Give the position of every malaria parasite and every leukocyte.
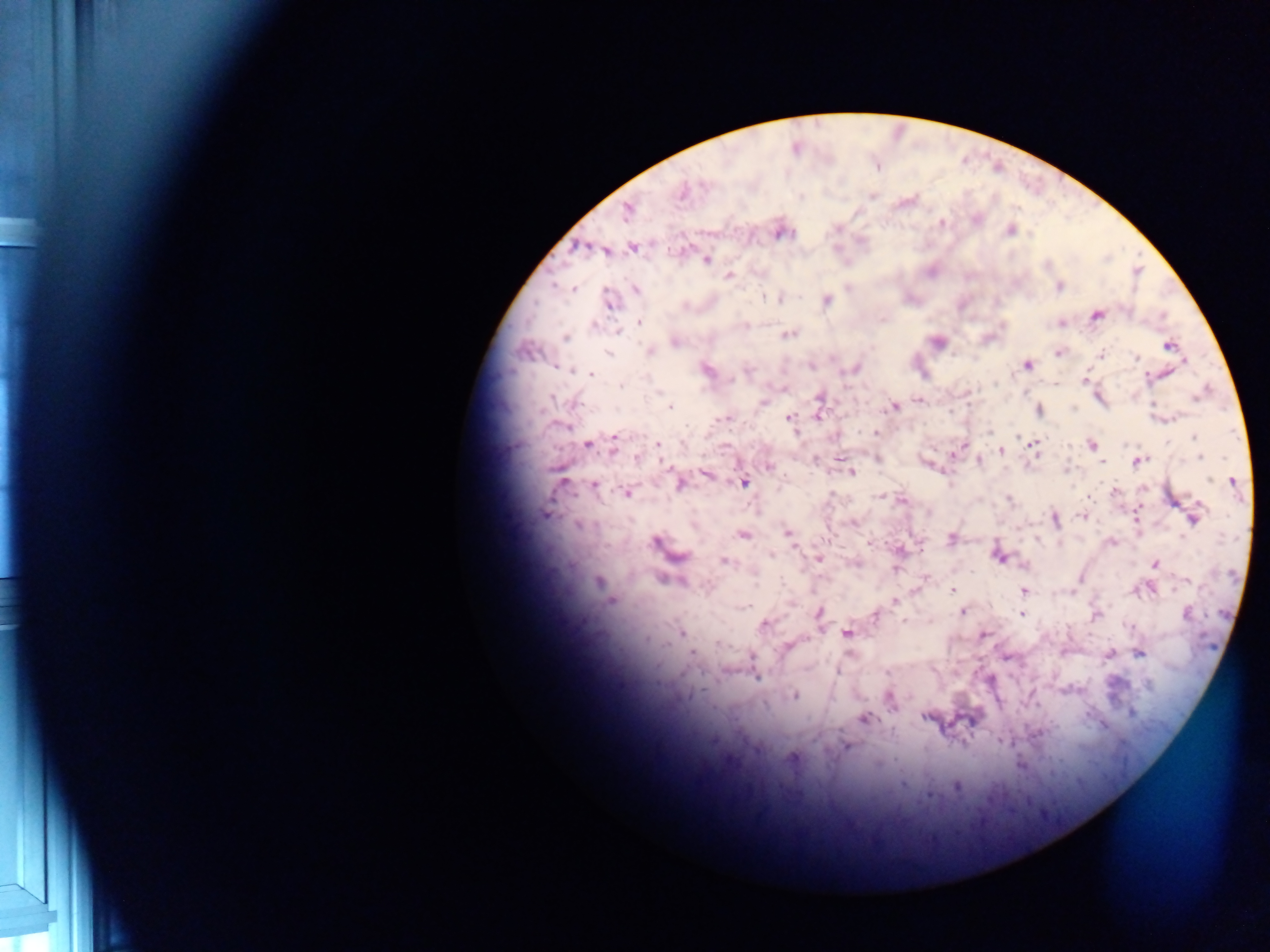

Approximate centers as {x, y} in pixels.
Malaria parasites: {681, 193}, {870, 194}, {905, 201}, {627, 210}, {975, 218}, {941, 223}, {1010, 229}, {779, 231}, {583, 247}, {604, 248}, {633, 248}, {706, 259}, {728, 275}, {1059, 286}, {635, 288}, {572, 289}, {779, 298}, {825, 300}, {608, 301}, {1096, 315}, {1060, 321}, {638, 322}, {745, 325}, {788, 334}, {566, 337}, {675, 341}, {937, 342}, {1168, 345}, {649, 351}, {1059, 351}, {607, 352}, {1101, 355}, {1135, 358}, {1027, 364}, {810, 365}, {854, 368}, {706, 369}, {590, 374}, {1084, 381}, {1054, 383}, {782, 388}, {820, 397}, {919, 400}, {763, 403}, {892, 406}, {669, 407}, {1038, 410}, {819, 414}, {726, 417}, {790, 418}, {875, 433}, {587, 444}, {656, 444}, {1091, 444}, {613, 445}, {1032, 445}, {1001, 449}, {1200, 456}, {637, 457}, {837, 457}, {876, 458}, {979, 460}, {1138, 461}, {926, 462}, {1102, 462}, {769, 466}, {851, 472}, {705, 474}, {1233, 481}, {678, 482}, {744, 482}, {593, 485}, {1114, 491}, {626, 492}, {881, 496}, {1172, 498}, {902, 500}, {544, 514}, {1136, 515}, {1083, 516}, {1194, 517}, {1055, 519}, {852, 523}, {787, 533}, {742, 534}, {951, 538}, {869, 541}, {1111, 542}, {656, 543}, {899, 550}, {999, 556}, {819, 557}, {724, 560}, {856, 563}, {1155, 564}, {896, 568}, {924, 577}, {668, 579}, {598, 582}, {952, 590}, {1023, 590}, {610, 601}, {894, 601}, {746, 605}, {963, 611}, {818, 613}, {1019, 613}, {874, 614}, {1095, 616}, {904, 621}, {763, 625}, {681, 632}, {847, 633}, {984, 634}, {787, 646}, {850, 651}, {1139, 653}, {693, 654}, {1109, 654}, {1004, 656}, {755, 676}, {794, 695}, {890, 700}, {1132, 713}, {926, 715}, {864, 718}, {999, 740}, {847, 745}, {792, 757}, {1020, 764}, {956, 785}, {931, 794}.
No leukocytes observed.

One field of view. Image is 1270×952 pixels. Sample from Ghana. Thick blood film. Mobile-phone photograph taken through the microscope.